State the blood parasite species.
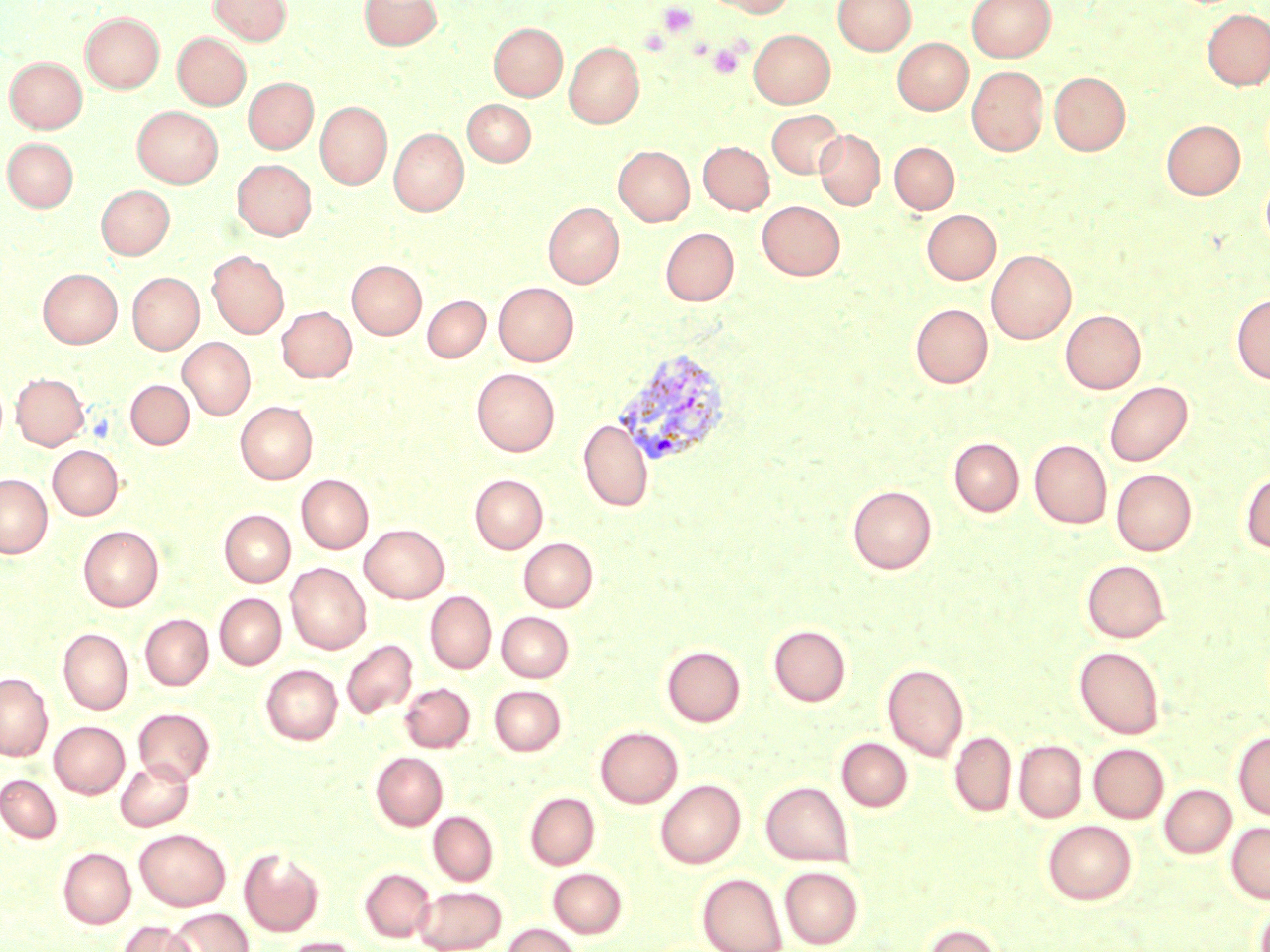

Plasmodium vivax.

Approximate bounding boxes as named x1/y1/x2/y2 corners in pixels. Uninfected red blood cell locations: (x1=210, y1=0, x2=291, y2=44), (x1=360, y1=0, x2=442, y2=50), (x1=707, y1=0, x2=795, y2=17), (x1=833, y1=0, x2=916, y2=55), (x1=967, y1=0, x2=1055, y2=62), (x1=1202, y1=9, x2=1270, y2=89), (x1=81, y1=12, x2=164, y2=93), (x1=489, y1=22, x2=567, y2=100), (x1=749, y1=29, x2=835, y2=108), (x1=173, y1=33, x2=250, y2=109), (x1=892, y1=38, x2=972, y2=114), (x1=564, y1=42, x2=644, y2=128), (x1=5, y1=57, x2=86, y2=133), (x1=967, y1=66, x2=1048, y2=155), (x1=1049, y1=72, x2=1130, y2=156), (x1=244, y1=78, x2=318, y2=153), (x1=463, y1=99, x2=535, y2=166), (x1=315, y1=101, x2=392, y2=189), (x1=132, y1=105, x2=223, y2=188), (x1=767, y1=109, x2=845, y2=179), (x1=1161, y1=120, x2=1245, y2=200), (x1=389, y1=128, x2=468, y2=216), (x1=814, y1=130, x2=884, y2=210), (x1=3, y1=138, x2=78, y2=211), (x1=698, y1=141, x2=774, y2=214), (x1=890, y1=142, x2=959, y2=213), (x1=614, y1=146, x2=694, y2=225), (x1=232, y1=160, x2=316, y2=239), (x1=1261, y1=172, x2=1270, y2=253), (x1=96, y1=185, x2=174, y2=259), (x1=757, y1=200, x2=845, y2=280), (x1=543, y1=202, x2=624, y2=288), (x1=922, y1=209, x2=1001, y2=284), (x1=660, y1=227, x2=738, y2=305), (x1=986, y1=249, x2=1076, y2=343), (x1=207, y1=251, x2=289, y2=338), (x1=347, y1=260, x2=426, y2=339), (x1=38, y1=268, x2=122, y2=346), (x1=128, y1=272, x2=204, y2=354), (x1=494, y1=282, x2=579, y2=366), (x1=1232, y1=293, x2=1270, y2=384), (x1=423, y1=295, x2=490, y2=362), (x1=910, y1=303, x2=992, y2=388), (x1=277, y1=306, x2=357, y2=382), (x1=1060, y1=309, x2=1146, y2=393), (x1=178, y1=337, x2=255, y2=419), (x1=472, y1=368, x2=560, y2=456), (x1=12, y1=372, x2=89, y2=450), (x1=126, y1=380, x2=194, y2=449), (x1=1104, y1=381, x2=1192, y2=466), (x1=235, y1=400, x2=317, y2=484), (x1=578, y1=419, x2=653, y2=512), (x1=949, y1=437, x2=1024, y2=516), (x1=1029, y1=439, x2=1112, y2=528), (x1=47, y1=445, x2=123, y2=520), (x1=1111, y1=469, x2=1196, y2=555), (x1=1240, y1=470, x2=1270, y2=553), (x1=470, y1=474, x2=548, y2=553), (x1=0, y1=475, x2=52, y2=557), (x1=296, y1=475, x2=373, y2=553), (x1=847, y1=485, x2=937, y2=574), (x1=219, y1=509, x2=295, y2=586), (x1=360, y1=524, x2=449, y2=603), (x1=78, y1=525, x2=164, y2=611), (x1=519, y1=537, x2=598, y2=611), (x1=1082, y1=559, x2=1170, y2=642), (x1=285, y1=562, x2=371, y2=654), (x1=425, y1=590, x2=496, y2=673), (x1=215, y1=593, x2=286, y2=669), (x1=496, y1=612, x2=573, y2=682), (x1=140, y1=614, x2=213, y2=690), (x1=768, y1=624, x2=851, y2=707), (x1=58, y1=628, x2=133, y2=714), (x1=341, y1=639, x2=417, y2=719), (x1=662, y1=645, x2=745, y2=726), (x1=1074, y1=646, x2=1166, y2=739), (x1=882, y1=663, x2=968, y2=761), (x1=261, y1=664, x2=342, y2=744), (x1=0, y1=672, x2=53, y2=761), (x1=400, y1=683, x2=474, y2=752), (x1=400, y1=685, x2=565, y2=752), (x1=489, y1=685, x2=566, y2=755), (x1=133, y1=707, x2=215, y2=785), (x1=49, y1=721, x2=129, y2=798), (x1=595, y1=727, x2=682, y2=808), (x1=949, y1=731, x2=1016, y2=817), (x1=1233, y1=732, x2=1270, y2=821), (x1=836, y1=738, x2=913, y2=811), (x1=1014, y1=740, x2=1087, y2=822), (x1=1089, y1=743, x2=1169, y2=823), (x1=371, y1=752, x2=447, y2=830), (x1=116, y1=759, x2=193, y2=830), (x1=0, y1=774, x2=62, y2=843), (x1=656, y1=779, x2=745, y2=868), (x1=761, y1=781, x2=854, y2=866), (x1=1160, y1=784, x2=1236, y2=858), (x1=525, y1=792, x2=600, y2=869), (x1=428, y1=811, x2=497, y2=885), (x1=1043, y1=820, x2=1137, y2=904), (x1=1226, y1=822, x2=1270, y2=904), (x1=135, y1=828, x2=231, y2=911), (x1=58, y1=848, x2=136, y2=928), (x1=239, y1=848, x2=324, y2=936), (x1=779, y1=866, x2=863, y2=948), (x1=359, y1=867, x2=435, y2=942), (x1=548, y1=867, x2=627, y2=938), (x1=697, y1=872, x2=787, y2=952), (x1=414, y1=886, x2=507, y2=952), (x1=1254, y1=899, x2=1270, y2=952), (x1=166, y1=909, x2=253, y2=952), (x1=120, y1=920, x2=196, y2=952), (x1=921, y1=923, x2=1003, y2=952), (x1=503, y1=924, x2=581, y2=952), (x1=283, y1=936, x2=362, y2=952). Plasmodium vivax-infected red blood cell locations: (x1=612, y1=347, x2=733, y2=470). Platelet locations: (x1=658, y1=2, x2=697, y2=37), (x1=708, y1=42, x2=744, y2=78). Image is 1270×952 pixels. Captured at 1000x magnification. Single field of view. Thin blood smear. Optical microscopy. May-Grünwald-Giemsa-stained preparation.